Locate every Plasmodium ovale-infected red blood cell.
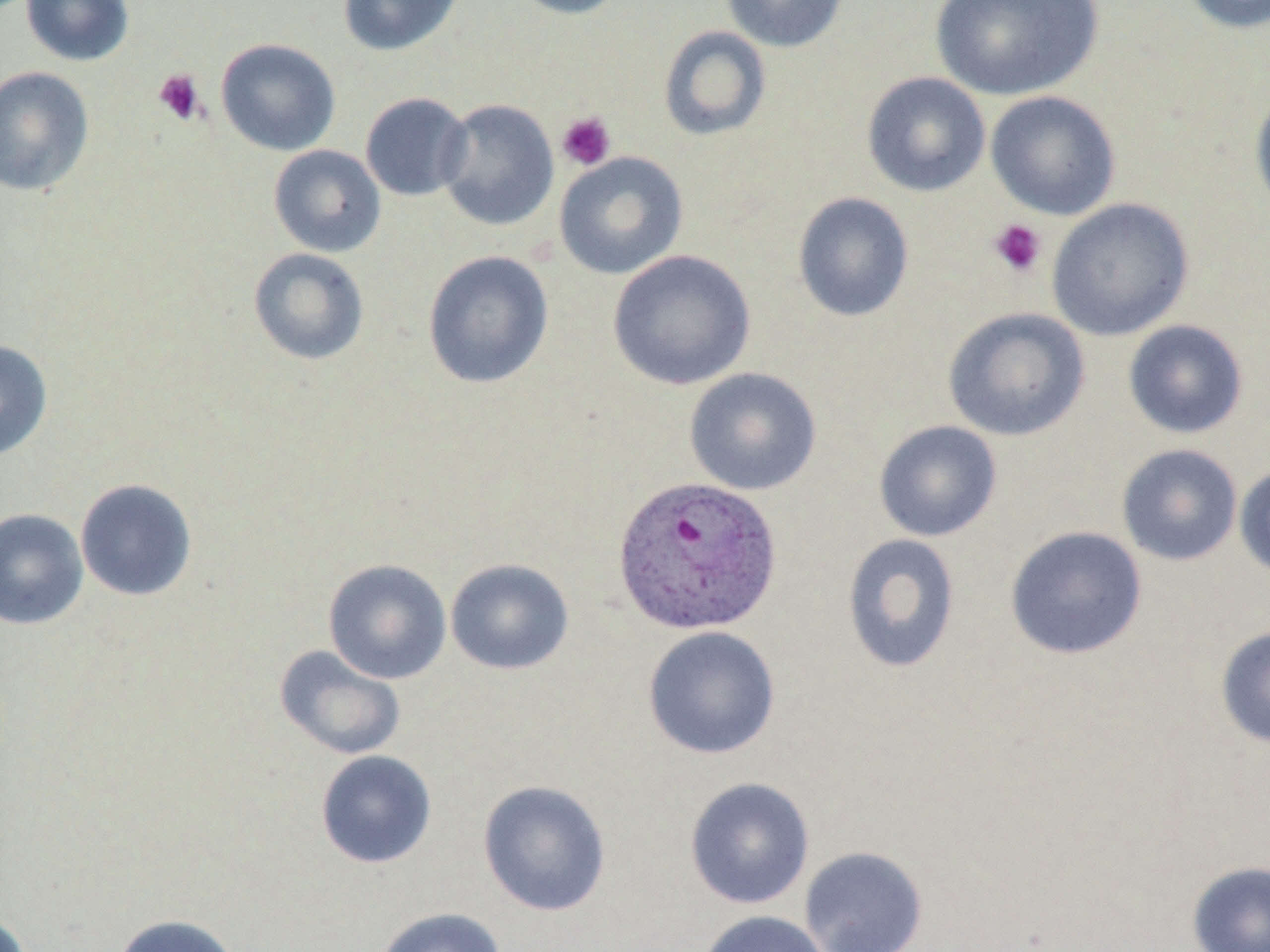

Approximate bounding boxes as [x1, y1, x2, y2] in pixels.
Plasmodium ovale-infected red blood cells: [612, 474, 783, 635].

Uninfected red blood cell locations: [20, 0, 135, 66], [337, 0, 465, 56], [506, 0, 630, 19], [721, 0, 849, 53], [931, 0, 1103, 101], [1180, 0, 1270, 35], [658, 25, 771, 141], [216, 38, 340, 156], [0, 66, 95, 196], [861, 72, 991, 197], [1248, 82, 1270, 224], [985, 90, 1121, 220], [360, 92, 473, 201], [436, 98, 559, 231], [268, 144, 386, 257], [554, 151, 689, 280], [792, 192, 914, 322], [1046, 198, 1195, 341], [248, 247, 369, 365], [606, 249, 757, 391], [422, 251, 554, 390], [942, 307, 1091, 441], [1122, 319, 1249, 439], [0, 340, 52, 462], [683, 367, 822, 496], [873, 420, 1003, 542], [1116, 443, 1243, 566], [1233, 463, 1270, 581], [74, 478, 197, 601], [0, 508, 88, 630], [1004, 525, 1147, 660], [841, 532, 961, 674], [322, 558, 452, 684], [445, 558, 575, 675], [642, 625, 781, 760], [1215, 625, 1270, 749], [274, 644, 406, 761], [315, 750, 437, 868], [684, 777, 815, 910], [477, 780, 611, 917], [799, 845, 929, 952], [1186, 860, 1270, 952], [371, 907, 506, 952], [696, 910, 833, 952], [0, 911, 32, 952], [112, 913, 240, 952]. Platelet locations: [153, 69, 206, 126], [556, 111, 616, 171], [989, 219, 1046, 277]. Slide-level diagnosis: Plasmodium ovale. May-Grünwald-Giemsa-stained preparation. Image is 1270×952 pixels. Thin blood film. Optical microscopy. One field of a larger specimen. 1000x magnification.